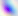
{
  "identification": "Toxoplasma gondii",
  "modality": "photomicrograph",
  "magnification": "400x"
}